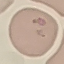

malaria status = parasitized
preparation = thin blood smear
stain = Giemsa
image type = cell patch, automatically extracted from a larger field of view and resized to 64 × 64 pixels
capture = smartphone camera at the microscope eyepiece